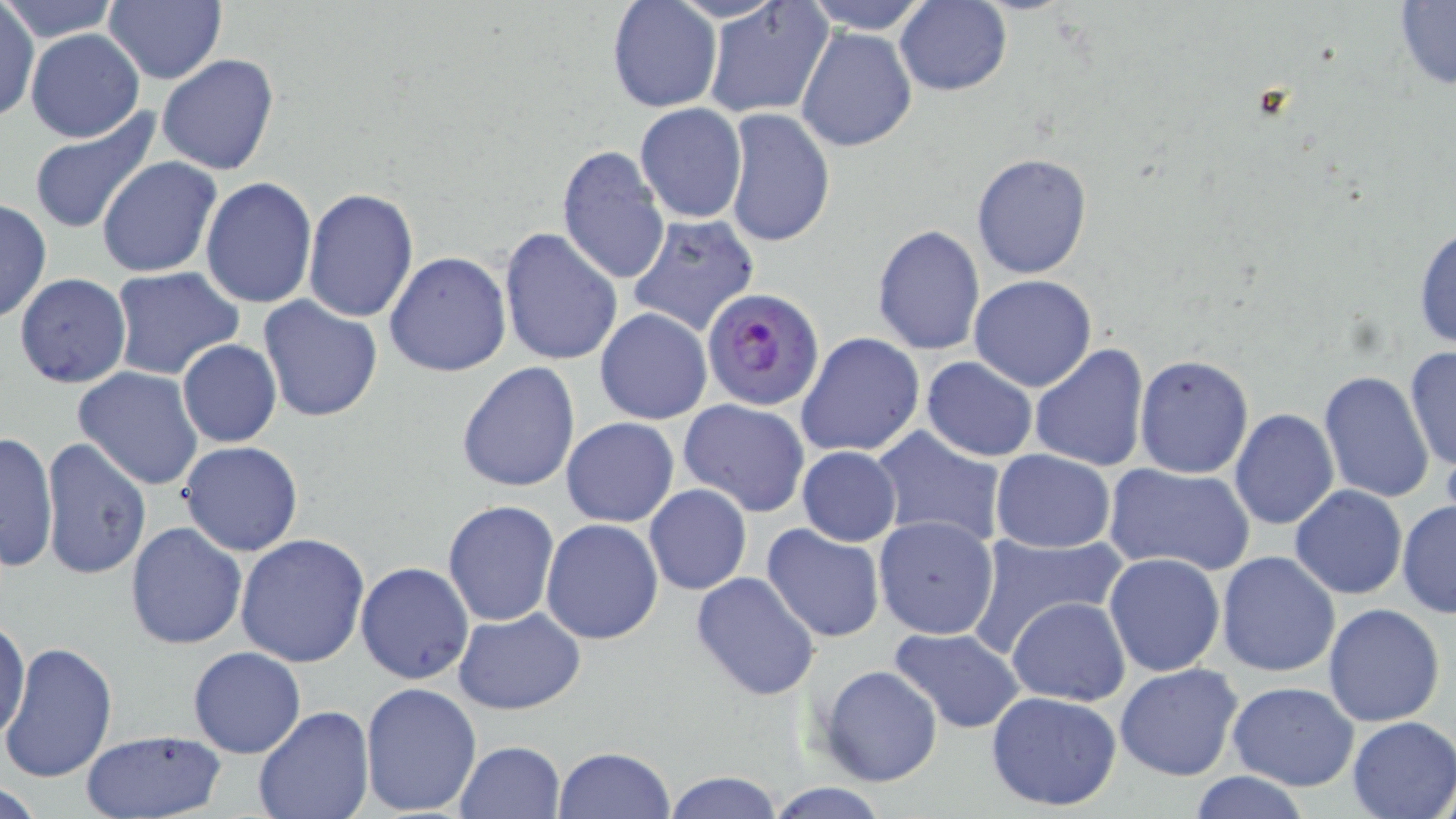

Approximate bounding boxes as named x1/y1/x2/y2 corners in pixels. Uninfected red blood cell locations: (x1=2, y1=0, x2=120, y2=41), (x1=606, y1=0, x2=722, y2=114), (x1=703, y1=0, x2=833, y2=119), (x1=803, y1=0, x2=931, y2=33), (x1=1392, y1=1, x2=1456, y2=90), (x1=104, y1=2, x2=227, y2=84), (x1=896, y1=2, x2=1012, y2=96), (x1=1, y1=4, x2=39, y2=123), (x1=796, y1=25, x2=918, y2=152), (x1=24, y1=28, x2=145, y2=143), (x1=156, y1=53, x2=281, y2=175), (x1=634, y1=104, x2=746, y2=222), (x1=724, y1=109, x2=835, y2=250), (x1=28, y1=113, x2=161, y2=233), (x1=556, y1=145, x2=671, y2=287), (x1=972, y1=153, x2=1092, y2=280), (x1=96, y1=156, x2=222, y2=278), (x1=199, y1=177, x2=318, y2=308), (x1=302, y1=187, x2=418, y2=325), (x1=0, y1=196, x2=51, y2=325), (x1=625, y1=214, x2=760, y2=337), (x1=1412, y1=219, x2=1456, y2=353), (x1=871, y1=224, x2=986, y2=357), (x1=498, y1=226, x2=622, y2=366), (x1=384, y1=252, x2=511, y2=376), (x1=108, y1=268, x2=245, y2=381), (x1=13, y1=273, x2=131, y2=389), (x1=968, y1=275, x2=1096, y2=392), (x1=258, y1=297, x2=383, y2=424), (x1=594, y1=309, x2=712, y2=426), (x1=796, y1=333, x2=926, y2=458), (x1=176, y1=340, x2=282, y2=448), (x1=1027, y1=341, x2=1149, y2=471), (x1=1404, y1=344, x2=1456, y2=475), (x1=1134, y1=355, x2=1254, y2=479), (x1=921, y1=356, x2=1038, y2=461), (x1=456, y1=360, x2=581, y2=492), (x1=71, y1=367, x2=204, y2=493), (x1=1317, y1=370, x2=1436, y2=503), (x1=680, y1=399, x2=809, y2=517), (x1=1229, y1=409, x2=1339, y2=530), (x1=561, y1=417, x2=679, y2=528), (x1=870, y1=425, x2=1008, y2=546), (x1=0, y1=430, x2=58, y2=576), (x1=39, y1=437, x2=153, y2=581), (x1=177, y1=440, x2=304, y2=558), (x1=796, y1=447, x2=902, y2=546), (x1=991, y1=450, x2=1115, y2=553), (x1=1104, y1=463, x2=1255, y2=576), (x1=643, y1=485, x2=751, y2=596), (x1=1290, y1=485, x2=1407, y2=599), (x1=1397, y1=499, x2=1456, y2=618), (x1=443, y1=500, x2=559, y2=627), (x1=874, y1=516, x2=999, y2=640), (x1=541, y1=518, x2=665, y2=645), (x1=125, y1=520, x2=248, y2=651), (x1=761, y1=522, x2=888, y2=643), (x1=965, y1=530, x2=1129, y2=655), (x1=235, y1=533, x2=370, y2=668), (x1=1217, y1=551, x2=1340, y2=678), (x1=1103, y1=552, x2=1227, y2=678), (x1=353, y1=562, x2=473, y2=684), (x1=690, y1=572, x2=820, y2=701), (x1=1006, y1=595, x2=1129, y2=705), (x1=1323, y1=602, x2=1447, y2=726), (x1=453, y1=608, x2=587, y2=713), (x1=1, y1=615, x2=29, y2=743), (x1=889, y1=627, x2=1026, y2=732), (x1=2, y1=643, x2=118, y2=783), (x1=189, y1=646, x2=306, y2=759), (x1=1114, y1=663, x2=1244, y2=781), (x1=818, y1=664, x2=943, y2=787), (x1=1225, y1=680, x2=1361, y2=792), (x1=359, y1=681, x2=484, y2=816), (x1=985, y1=690, x2=1124, y2=813), (x1=251, y1=706, x2=374, y2=819), (x1=1347, y1=716, x2=1454, y2=819), (x1=79, y1=728, x2=227, y2=819), (x1=452, y1=741, x2=565, y2=819), (x1=551, y1=747, x2=675, y2=819), (x1=664, y1=769, x2=783, y2=818), (x1=1187, y1=772, x2=1314, y2=818), (x1=2, y1=779, x2=50, y2=817), (x1=765, y1=782, x2=892, y2=818). Plasmodium falciparum-infected red blood cell locations: (x1=702, y1=287, x2=826, y2=411). Slide-level diagnosis: Plasmodium falciparum. May-Grünwald-Giemsa-stained preparation. Captured at 1000x magnification. Image is 1456×819 pixels. Single field of view. Thin blood film. Optical microscopy.